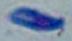
modality = photomicrograph
identification = Toxoplasma gondii
magnification = 1000x